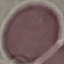

Malaria status: uninfected. Giemsa-stained preparation. Acquired by smartphone through the microscope eyepiece. Automatically extracted cell patch, resized to 64 × 64 pixels. Thin smear of blood.